Report the malaria status of this cell.
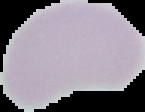
Uninfected.

From a thin blood smear. Image is 145×112 pixels. Segmented cell region on a black background.